Identify the parasite.
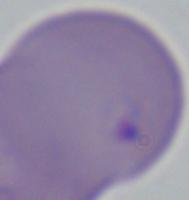
Babesia.

Summary:
  - Magnification: 1000x
  - Modality: photomicrograph